Assess for Plasmodium parasites.
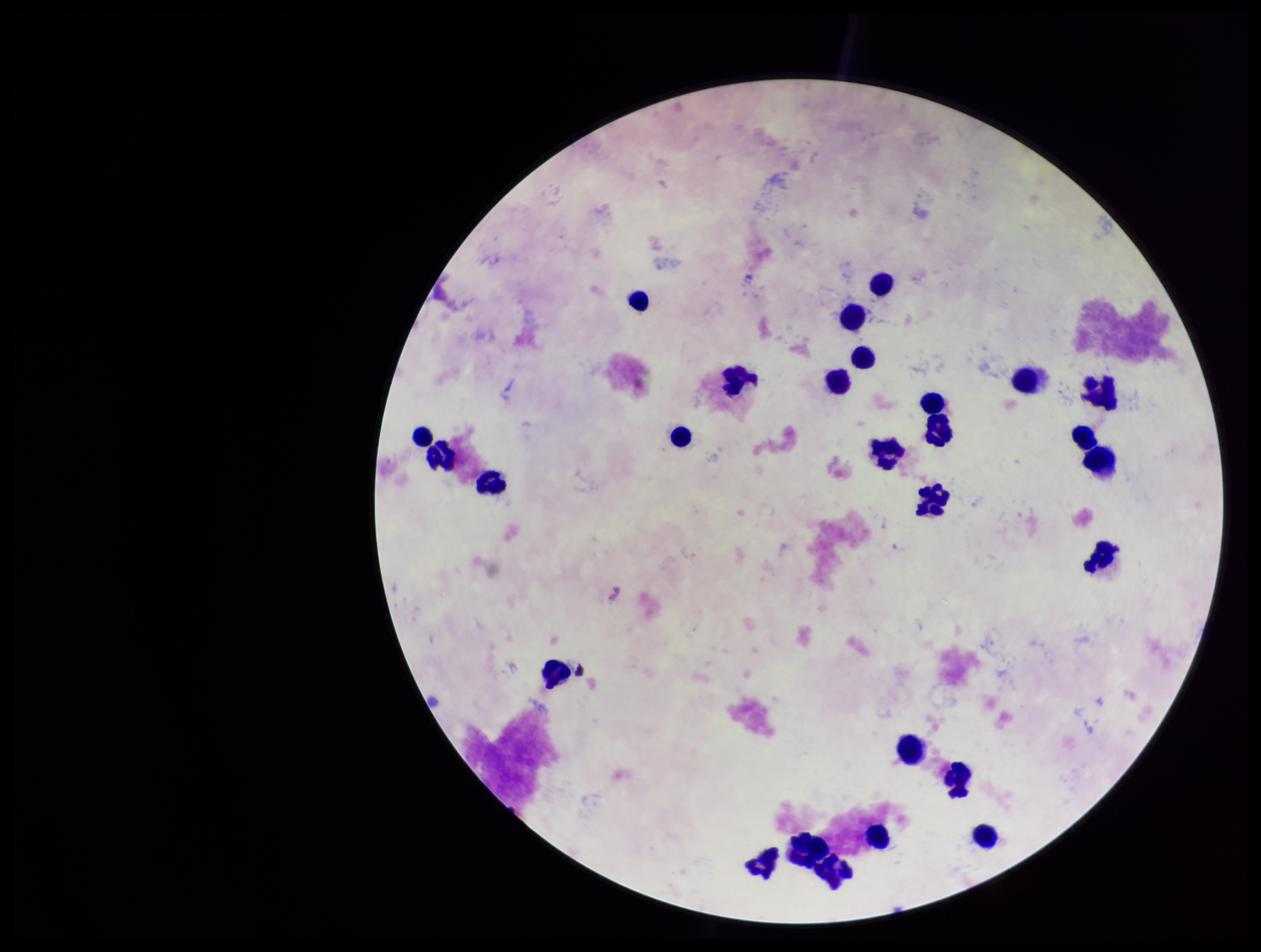
None identified.

capture = smartphone photograph through the microscope eyepiece
stain = Giemsa
parasite count = 0
patient malaria status = negative
preparation = thick
field of view = single
image size = 1261×952 pixels
leukocyte count = 27